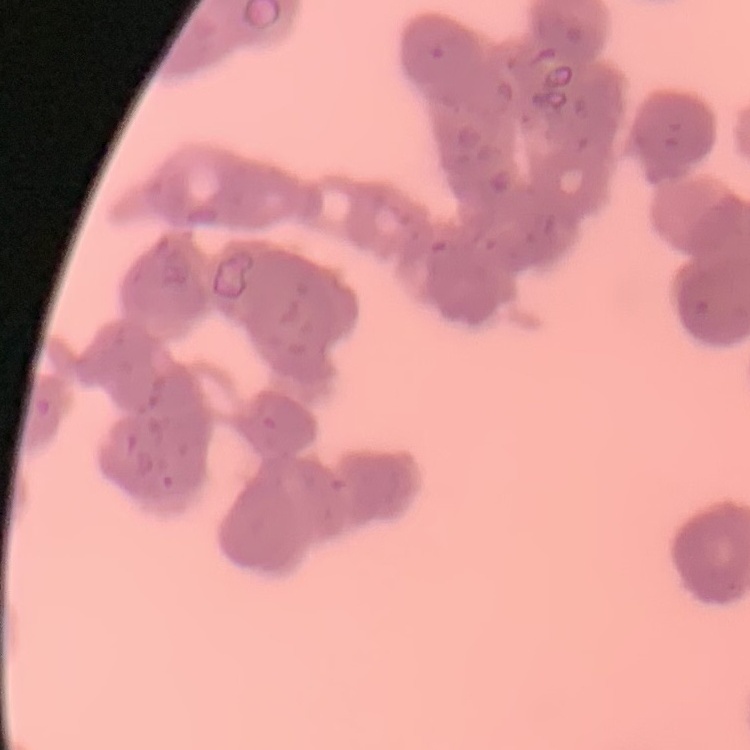
Summary:
  - Red blood cell morphology: rouleaux formation
  - Stain: Field's or Giemsa
  - Preparation: thin peripheral smear
  - Image type: one tile cut from a larger photomicrograph